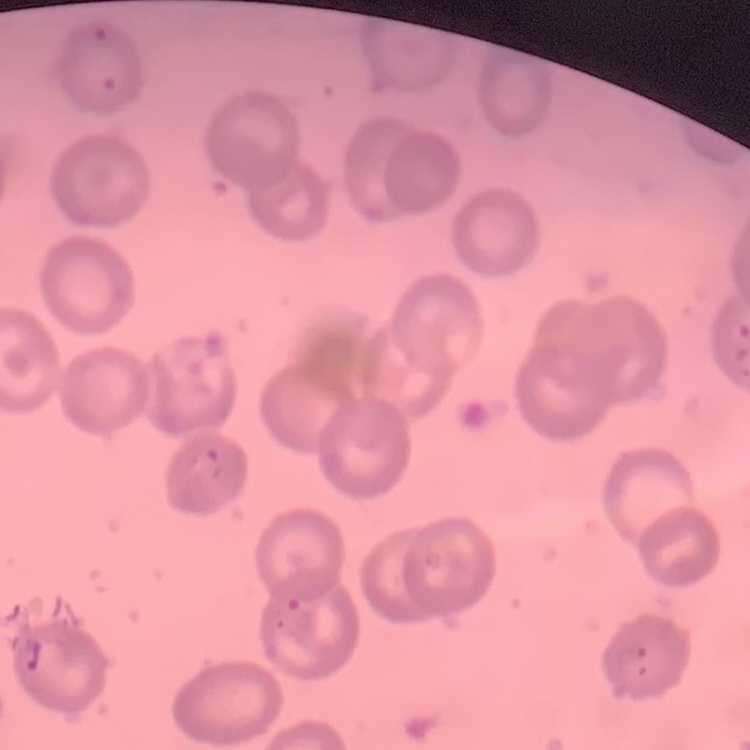

red blood cell morphology = no rouleaux formation
preparation = thin peripheral smear
stain = Field's or Giemsa
image type = square crop of a larger photomicrograph